Report the malaria status of this cell.
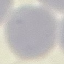

It is uninfected.

stain: Giemsa
image_type: cell patch, automatically extracted from a larger field of view and resized to 64 × 64 pixels
capture: smartphone through the microscope eyepiece
preparation: thin smear